Locate every blood parasite and identify its species.
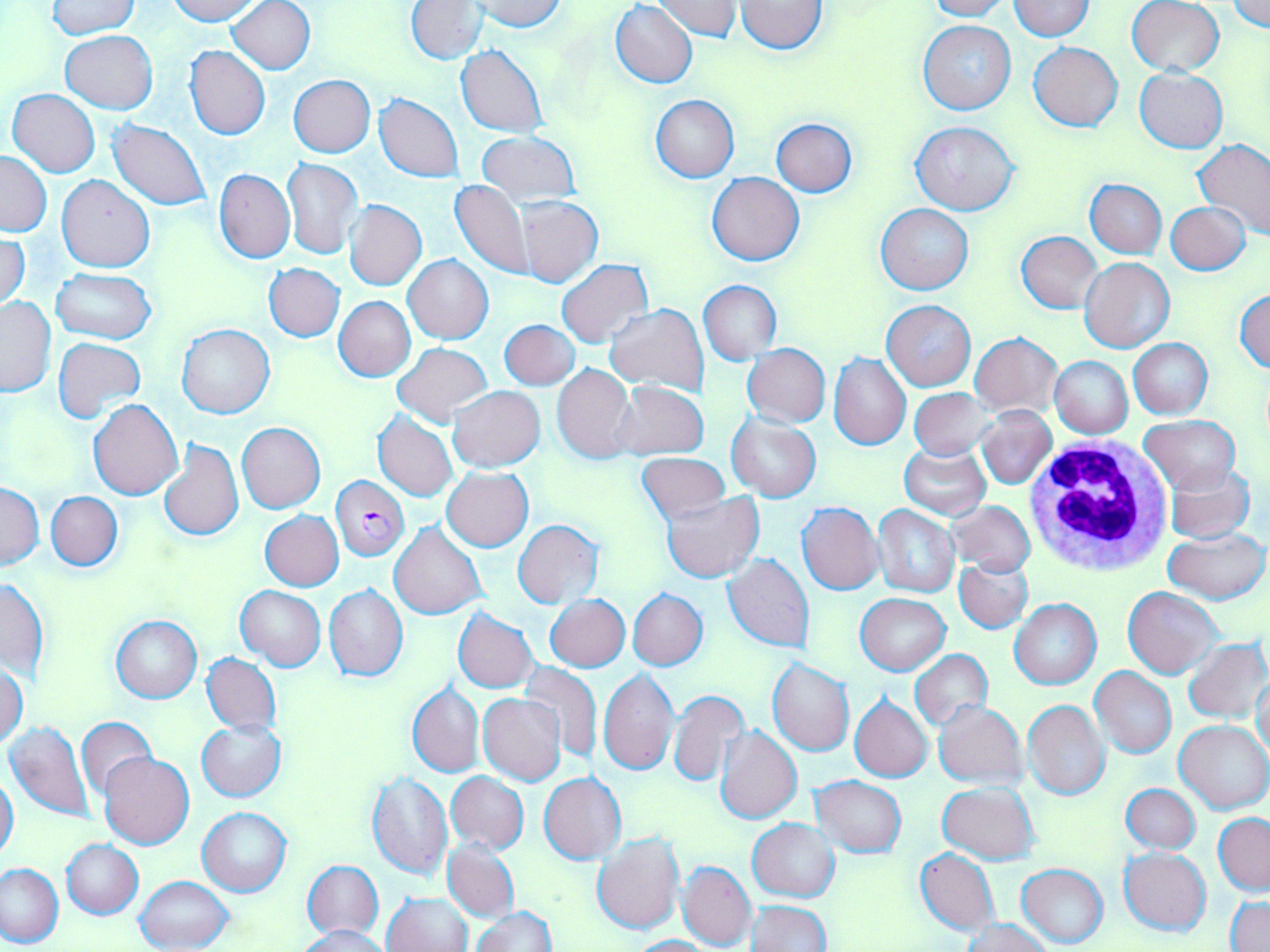

Approximate bounding boxes as (x1, y1, x2, y2) in pixels.
Plasmodium falciparum-infected red blood cells: (330, 475, 409, 561).
No Plasmodium ovale, Plasmodium malariae, Plasmodium vivax, Babesia divergens, or Trypanosoma brucei observed.

slide-level diagnosis = Plasmodium falciparum
field of view = one of a larger specimen
magnification = 1000x
image size = 1270×952 pixels
uninfected red blood cell locations = approximate bounding boxes as (x1, y1, x2, y2) in pixels: (166, 0, 264, 24), (227, 0, 315, 74), (654, 0, 740, 41), (928, 0, 1007, 20), (1007, 0, 1094, 40), (1228, 0, 1270, 33), (405, 1, 486, 64), (474, 1, 566, 33), (736, 1, 827, 53), (1126, 1, 1225, 77), (47, 2, 141, 39), (610, 2, 698, 88), (917, 19, 1016, 115), (59, 30, 157, 114), (1029, 42, 1122, 132), (456, 45, 548, 136), (185, 46, 270, 140), (1133, 67, 1227, 153), (288, 75, 375, 156), (7, 89, 100, 177), (375, 93, 463, 183), (650, 95, 739, 182), (771, 118, 857, 196), (108, 120, 211, 210), (912, 120, 1017, 216), (475, 130, 581, 207), (1193, 139, 1270, 241), (0, 152, 51, 236), (282, 158, 363, 260), (215, 169, 295, 263), (707, 172, 805, 265), (56, 175, 154, 273), (1085, 179, 1166, 258), (450, 180, 531, 278), (512, 195, 603, 287), (346, 200, 427, 289), (1165, 202, 1250, 276), (877, 203, 972, 295), (1017, 231, 1101, 313), (0, 232, 30, 313), (404, 253, 493, 343), (1079, 257, 1176, 352), (556, 259, 653, 348), (264, 262, 344, 342), (52, 269, 155, 344), (698, 279, 782, 365), (1233, 287, 1270, 373), (0, 295, 56, 397), (334, 296, 415, 381), (882, 301, 975, 390), (605, 305, 708, 394), (499, 319, 579, 390), (177, 324, 273, 419), (970, 332, 1063, 416), (53, 338, 146, 423), (1128, 338, 1211, 418), (392, 342, 492, 428), (743, 343, 830, 427), (827, 352, 910, 450), (1050, 354, 1133, 439), (551, 363, 636, 463), (610, 380, 708, 461), (449, 385, 544, 471), (910, 389, 994, 460), (88, 400, 183, 500), (976, 406, 1056, 489), (373, 412, 458, 501), (725, 414, 820, 502), (1140, 416, 1240, 494), (237, 422, 326, 513), (158, 439, 243, 540), (899, 444, 991, 519), (636, 453, 731, 524), (1166, 465, 1254, 543), (442, 466, 533, 551), (0, 484, 45, 570), (46, 491, 122, 570), (661, 493, 763, 582), (948, 501, 1036, 577), (796, 502, 884, 595), (873, 504, 959, 598), (260, 512, 344, 591), (513, 520, 605, 609), (389, 521, 487, 619), (1164, 528, 1269, 605), (723, 554, 813, 651), (954, 556, 1033, 634), (1, 577, 49, 679), (324, 585, 408, 682), (235, 586, 326, 671), (1122, 586, 1222, 678), (628, 589, 707, 670), (855, 594, 950, 674), (546, 595, 630, 671), (1009, 598, 1101, 690), (453, 608, 538, 693), (111, 616, 201, 703), (1183, 638, 1269, 724), (910, 649, 993, 731), (202, 653, 282, 735), (767, 659, 855, 756), (520, 663, 601, 764), (0, 664, 27, 749), (1090, 667, 1176, 759), (598, 668, 679, 777), (1253, 671, 1269, 766), (406, 682, 484, 777), (668, 689, 749, 788), (478, 693, 567, 785), (849, 695, 933, 782), (685, 698, 788, 810), (1022, 699, 1111, 801), (934, 701, 1026, 789), (75, 718, 157, 801), (4, 719, 95, 823), (197, 719, 287, 801), (1174, 720, 1270, 813), (716, 725, 802, 824), (99, 752, 194, 848), (447, 771, 529, 855), (567, 771, 626, 862), (366, 772, 452, 879), (539, 772, 605, 864), (0, 773, 19, 865), (811, 776, 906, 857), (938, 782, 1039, 864), (1121, 784, 1200, 855), (197, 807, 292, 896), (1214, 814, 1270, 895), (748, 818, 840, 901), (592, 832, 686, 935), (61, 839, 143, 918), (443, 839, 519, 921), (1120, 847, 1210, 935), (915, 849, 999, 935), (303, 860, 383, 939), (678, 861, 756, 950), (1016, 863, 1109, 948), (0, 864, 63, 947), (135, 875, 234, 952), (384, 892, 473, 952), (1226, 895, 1270, 952), (747, 899, 831, 951), (470, 907, 556, 952), (962, 918, 1051, 951), (298, 925, 389, 951), (629, 935, 715, 952)
white blood cell locations = approximate bounding boxes as (x1, y1, x2, y2) in pixels: (1024, 437, 1175, 579)
stain = May-Grünwald-Giemsa
modality = light microscopy
preparation = thin blood smear